Classify this cell by malaria status.
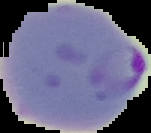
Parasitized.

Image is 151×133 pixels. From a thin blood film. The area outside the segmented cell region is set to black.